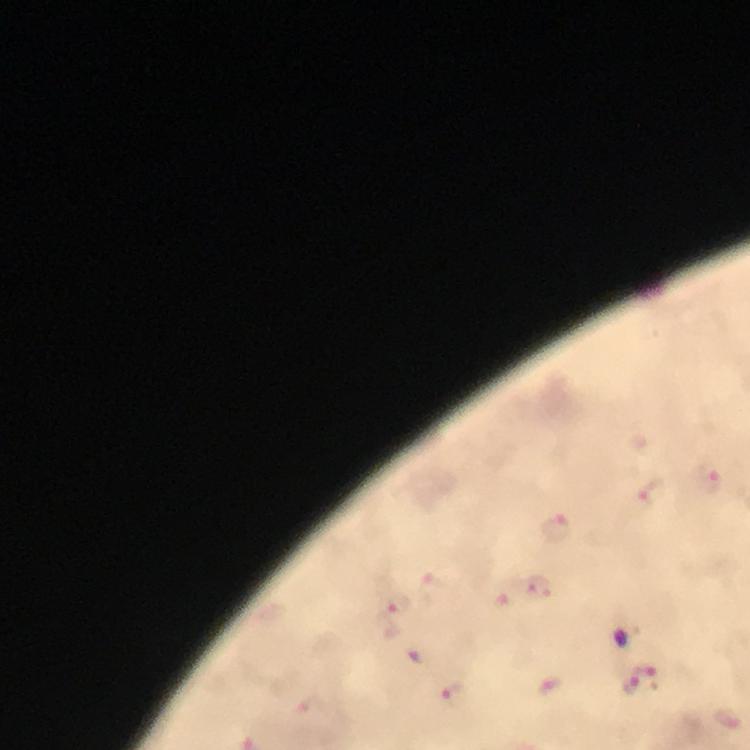

Approximate object centers, in pixels from the top-left corner. Plasmodium parasite locations: (x=713, y=479), (x=652, y=493), (x=555, y=526), (x=536, y=588), (x=396, y=608), (x=639, y=678), (x=452, y=693). From a malaria diagnostic workup. Image is 750×750 pixels. Immersion oil applied. Cropped region of a single field of view. Thick blood smear. 100x magnification. Giemsa stain. Photographed with a smartphone mounted on the microscope.